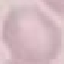
Result: negative for malaria parasites. Thin blood smear. Photographed with a smartphone camera at the microscope eyepiece. Giemsa-stained preparation. Cell patch, automatically extracted from a larger field of view and resized to 64 × 64 pixels.